Outline each blood parasite and name the species.
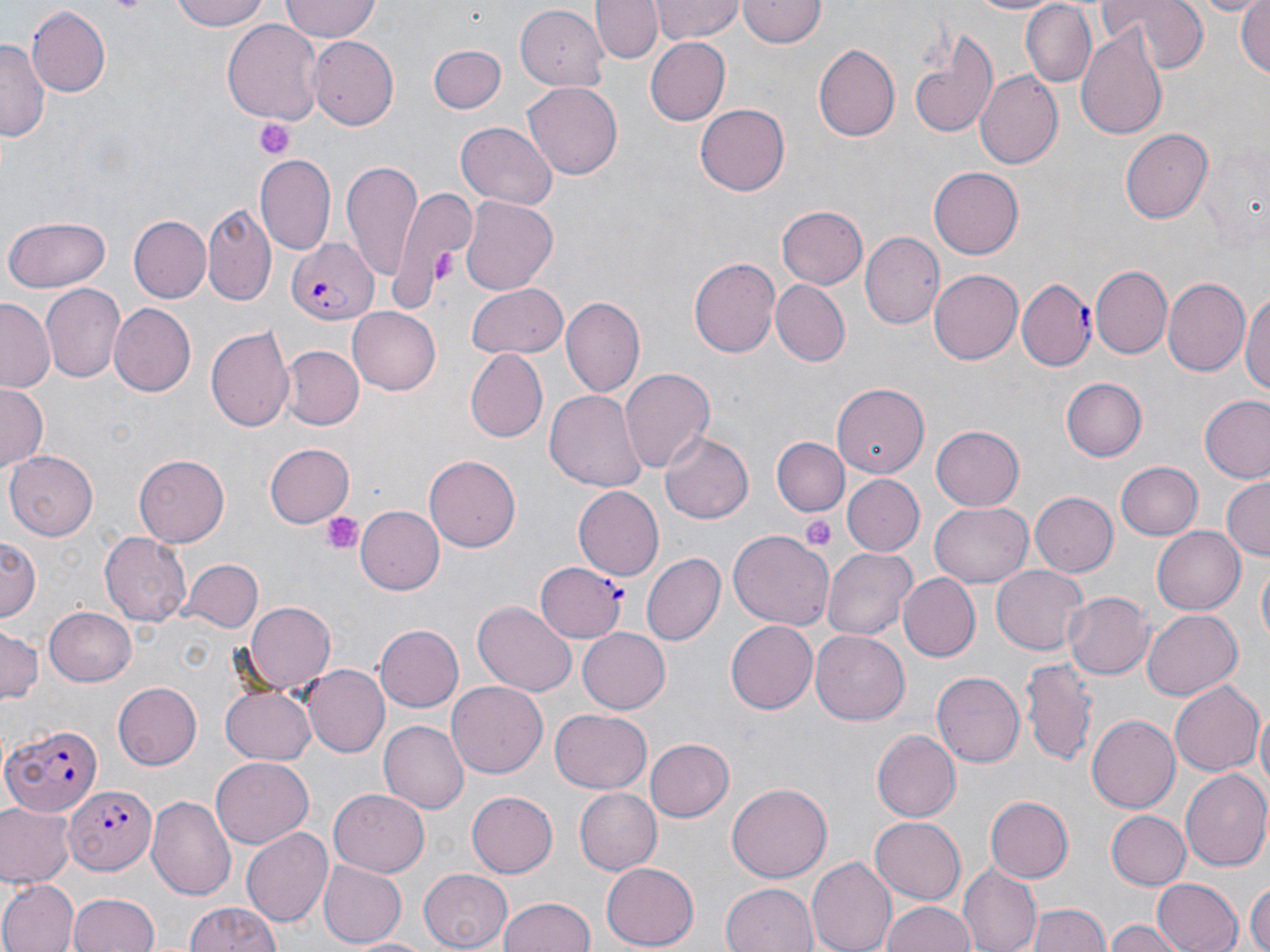

Approximate bounding boxes as (x1, y1, x2, y2) in pixels.
Plasmodium falciparum-infected red blood cells: (286, 238, 377, 323), (1017, 280, 1092, 370), (536, 562, 627, 641), (2, 723, 104, 815), (69, 782, 156, 875).
No Plasmodium ovale, Plasmodium malariae, Plasmodium vivax, Babesia divergens, or Trypanosoma brucei observed.

Summary:
  - Platelet locations: (253, 118, 296, 159), (423, 248, 455, 289), (319, 512, 363, 557), (800, 515, 837, 550)
  - Uninfected red blood cell locations: (170, 0, 271, 31), (279, 0, 383, 43), (591, 0, 663, 66), (649, 0, 744, 43), (739, 0, 826, 48), (967, 0, 1064, 16), (1099, 0, 1209, 71), (1188, 0, 1265, 17), (1235, 0, 1269, 83), (1020, 2, 1098, 88), (28, 7, 111, 97), (516, 7, 607, 92), (223, 18, 323, 128), (1074, 24, 1168, 144), (909, 31, 1002, 140), (308, 37, 399, 130), (645, 37, 730, 125), (0, 38, 44, 145), (813, 42, 899, 141), (428, 43, 507, 115), (974, 71, 1064, 170), (522, 81, 624, 180), (695, 103, 787, 196), (456, 122, 558, 211), (1120, 125, 1213, 221), (255, 153, 337, 255), (342, 160, 422, 286), (929, 166, 1024, 258), (391, 187, 476, 307), (460, 195, 558, 294), (203, 203, 275, 304), (776, 205, 868, 291), (4, 215, 113, 291), (129, 216, 210, 302), (860, 233, 943, 330), (688, 256, 780, 358), (1091, 266, 1172, 360), (929, 267, 1023, 360), (1164, 276, 1253, 376), (466, 280, 569, 359), (773, 280, 849, 365), (42, 285, 124, 383), (1242, 287, 1270, 405), (562, 299, 644, 394), (0, 300, 54, 393), (107, 302, 195, 396), (348, 309, 441, 395), (205, 324, 293, 435), (283, 346, 362, 429), (466, 352, 548, 440), (618, 368, 717, 473), (1060, 376, 1147, 461), (0, 382, 48, 470), (832, 384, 929, 478), (546, 390, 645, 493), (1199, 396, 1270, 483), (930, 424, 1025, 511), (661, 432, 753, 523), (772, 437, 849, 516), (263, 442, 355, 528), (4, 451, 100, 542), (134, 455, 230, 545), (424, 455, 520, 553), (1116, 461, 1203, 540), (842, 475, 922, 554), (1221, 477, 1269, 560), (574, 486, 664, 580), (1027, 491, 1117, 577), (931, 502, 1032, 586), (357, 505, 445, 594), (1152, 523, 1245, 612), (100, 531, 190, 626), (728, 531, 833, 631), (1, 537, 40, 621), (823, 546, 917, 641), (643, 553, 725, 645), (180, 559, 262, 634), (1255, 559, 1269, 651), (992, 566, 1087, 654), (899, 573, 981, 661), (1061, 591, 1149, 680), (472, 600, 577, 697), (244, 602, 337, 692), (43, 606, 138, 686), (1141, 607, 1242, 699), (726, 621, 818, 715), (375, 624, 464, 711), (0, 627, 42, 706), (579, 630, 670, 713), (812, 631, 910, 725), (1021, 656, 1099, 766), (301, 664, 390, 758), (931, 671, 1024, 768), (1167, 680, 1262, 777), (112, 682, 202, 770), (447, 682, 549, 777), (221, 685, 316, 765), (549, 709, 652, 794), (1256, 709, 1270, 805), (1088, 715, 1180, 812), (378, 720, 469, 814), (869, 729, 959, 823), (646, 738, 734, 821), (210, 758, 312, 848), (1181, 770, 1270, 873), (727, 781, 831, 882), (574, 786, 662, 875), (329, 787, 432, 876), (466, 791, 558, 879), (149, 795, 240, 899), (984, 797, 1071, 884), (0, 801, 75, 887), (1105, 810, 1190, 889), (870, 815, 966, 903), (243, 827, 333, 927), (805, 855, 895, 952), (318, 860, 407, 945), (600, 862, 700, 948), (960, 864, 1042, 952), (420, 867, 516, 948), (1152, 877, 1244, 952), (1245, 877, 1269, 952), (0, 879, 77, 952), (721, 883, 817, 952), (69, 891, 161, 952), (498, 896, 598, 952), (879, 899, 978, 952), (183, 900, 283, 952), (1030, 906, 1109, 952), (1107, 920, 1183, 952), (347, 935, 434, 952)
  - Slide-level diagnosis: Plasmodium falciparum
  - Modality: optical microscopy
  - Magnification: 1000x
  - Preparation: thin blood smear
  - Stain: May-Grünwald-Giemsa
  - Image size: 1270×952 pixels
  - Field of view: single